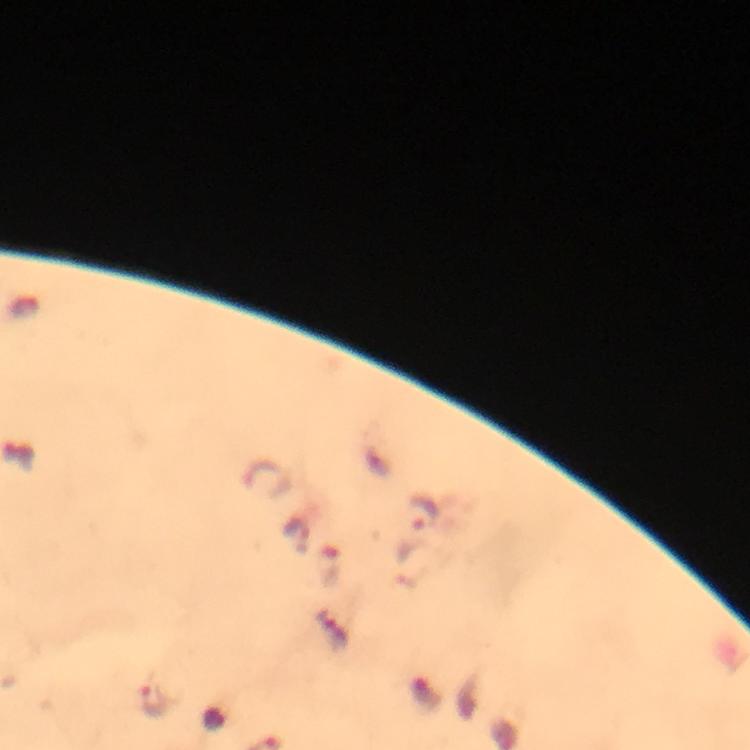

Approximate object centers, in pixels from the top-left corner. Plasmodium parasite locations: (x=427, y=513), (x=328, y=566), (x=153, y=697). A crop from one field of view. Thick blood film. Immersion oil was used. Image is 750×750 pixels. From a malaria diagnostic workup. Giemsa-stained preparation. Smartphone photograph taken through a microscope. At 100x magnification.